State the blood parasite species.
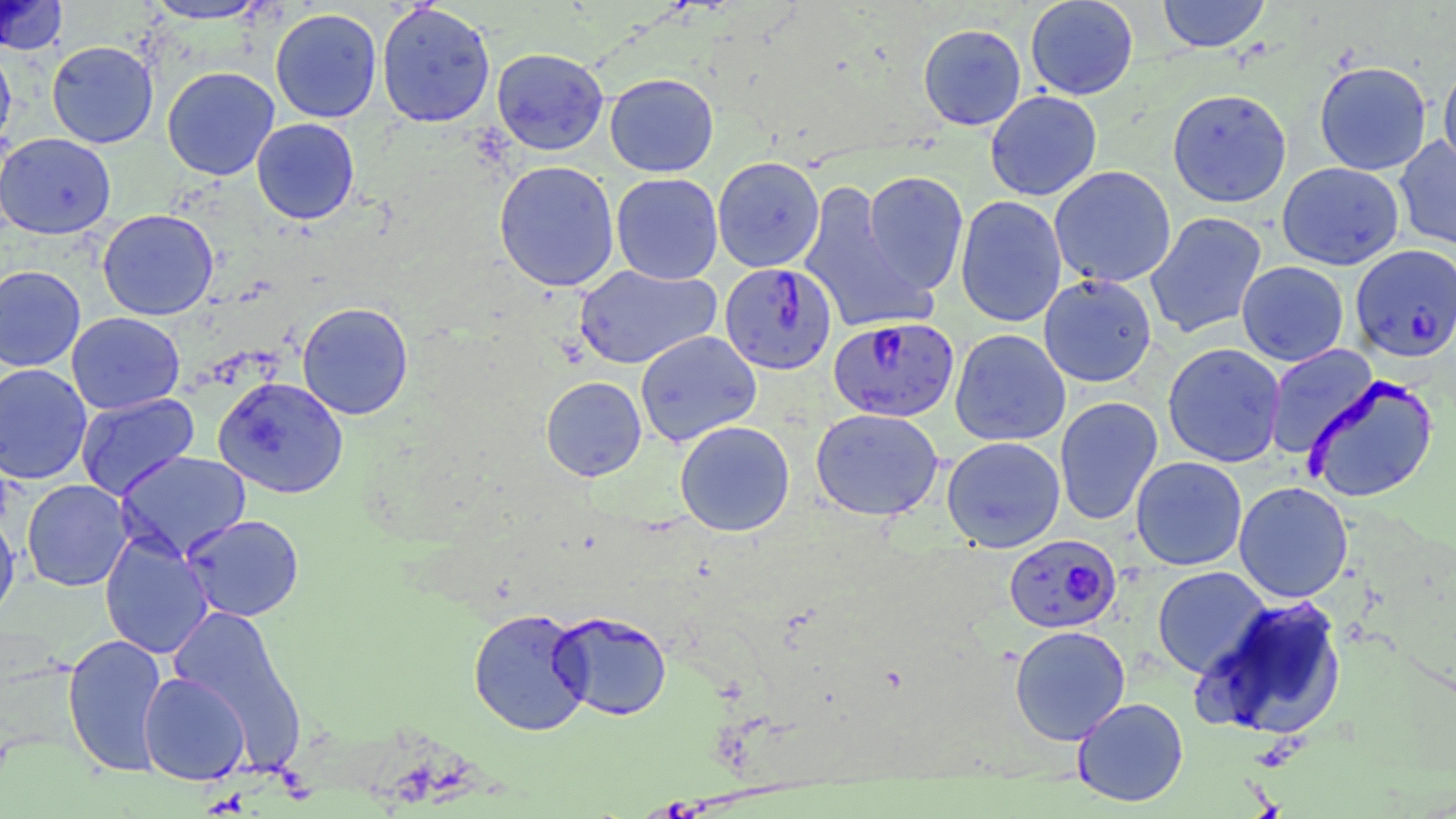
Plasmodium falciparum.

Summary:
  - Coordinate format: approximate bounding boxes as named x1/y1/x2/y2 corners in pixels
  - Plasmodium falciparum-infected red blood cell locations: (x1=1354, y1=244, x2=1456, y2=361), (x1=719, y1=261, x2=838, y2=375), (x1=828, y1=316, x2=959, y2=422), (x1=1004, y1=533, x2=1122, y2=634)
  - Uninfected red blood cell locations: (x1=0, y1=0, x2=68, y2=55), (x1=142, y1=0, x2=273, y2=24), (x1=1025, y1=0, x2=1139, y2=100), (x1=1156, y1=0, x2=1270, y2=52), (x1=376, y1=2, x2=496, y2=128), (x1=270, y1=7, x2=382, y2=123), (x1=918, y1=24, x2=1026, y2=131), (x1=46, y1=40, x2=159, y2=148), (x1=0, y1=43, x2=17, y2=154), (x1=492, y1=48, x2=608, y2=155), (x1=1314, y1=60, x2=1432, y2=175), (x1=1438, y1=60, x2=1456, y2=175), (x1=162, y1=66, x2=280, y2=181), (x1=604, y1=72, x2=719, y2=177), (x1=1167, y1=88, x2=1292, y2=208), (x1=985, y1=90, x2=1102, y2=201), (x1=251, y1=118, x2=360, y2=224), (x1=0, y1=132, x2=116, y2=239), (x1=1394, y1=135, x2=1456, y2=251), (x1=712, y1=156, x2=824, y2=273), (x1=494, y1=160, x2=619, y2=292), (x1=1277, y1=162, x2=1404, y2=270), (x1=1049, y1=166, x2=1176, y2=288), (x1=862, y1=171, x2=969, y2=294), (x1=611, y1=173, x2=723, y2=285), (x1=797, y1=179, x2=933, y2=336), (x1=955, y1=195, x2=1067, y2=328), (x1=97, y1=209, x2=219, y2=320), (x1=1145, y1=211, x2=1268, y2=339), (x1=1236, y1=261, x2=1349, y2=366), (x1=574, y1=264, x2=720, y2=369), (x1=0, y1=265, x2=85, y2=371), (x1=1038, y1=274, x2=1157, y2=387), (x1=297, y1=302, x2=413, y2=419), (x1=66, y1=312, x2=184, y2=415), (x1=950, y1=328, x2=1071, y2=446), (x1=635, y1=330, x2=761, y2=447), (x1=1162, y1=343, x2=1286, y2=468), (x1=1264, y1=345, x2=1378, y2=459), (x1=0, y1=363, x2=92, y2=484), (x1=1303, y1=375, x2=1438, y2=502), (x1=541, y1=376, x2=646, y2=481), (x1=213, y1=377, x2=349, y2=498), (x1=75, y1=392, x2=200, y2=499), (x1=1054, y1=396, x2=1163, y2=526), (x1=810, y1=407, x2=944, y2=521), (x1=675, y1=420, x2=795, y2=537), (x1=941, y1=436, x2=1066, y2=552), (x1=114, y1=451, x2=251, y2=561), (x1=1130, y1=456, x2=1248, y2=571), (x1=21, y1=479, x2=132, y2=591), (x1=1233, y1=481, x2=1353, y2=603), (x1=0, y1=512, x2=20, y2=625), (x1=182, y1=514, x2=304, y2=622), (x1=99, y1=532, x2=213, y2=659), (x1=1152, y1=566, x2=1272, y2=678), (x1=1195, y1=595, x2=1348, y2=740), (x1=165, y1=604, x2=307, y2=768), (x1=468, y1=607, x2=592, y2=736), (x1=550, y1=610, x2=673, y2=721), (x1=1009, y1=625, x2=1131, y2=745), (x1=62, y1=632, x2=169, y2=777), (x1=138, y1=671, x2=251, y2=785), (x1=1072, y1=697, x2=1189, y2=807)
  - Preparation: thin blood film
  - Image size: 1456×819 pixels
  - Magnification: 1000x
  - Modality: light microscopy
  - Stain: May-Grünwald-Giemsa
  - Field of view: single